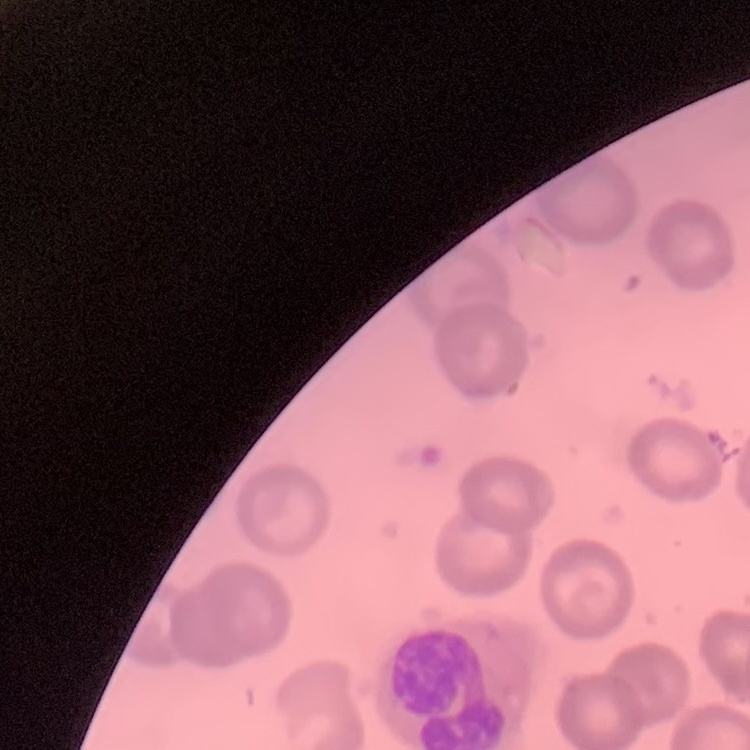 The red blood cells show no rouleaux formation. Field's or Giemsa stain. Square crop of a larger photomicrograph. Thin blood film.